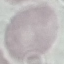
Result: no malaria parasites detected. Thin blood film. Cell patch, automatically extracted from a larger field of view and resized to 64 × 64 pixels. Acquired by smartphone through the microscope eyepiece. Giemsa-stained preparation.